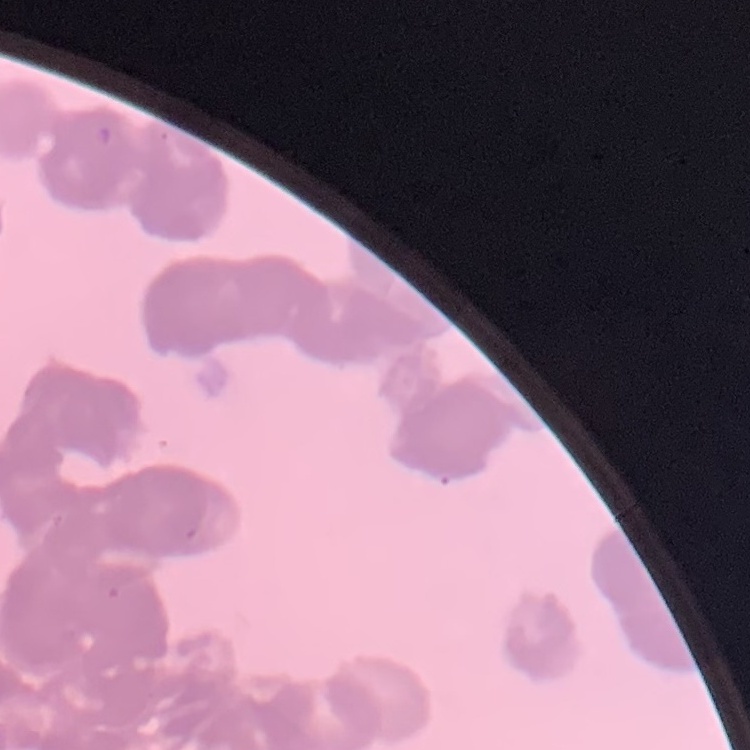

Summary:
  - Erythrocyte morphology: rouleaux formation
  - Image type: one tile cut from a larger photomicrograph
  - Stain: Field's or Giemsa
  - Preparation: thin blood smear